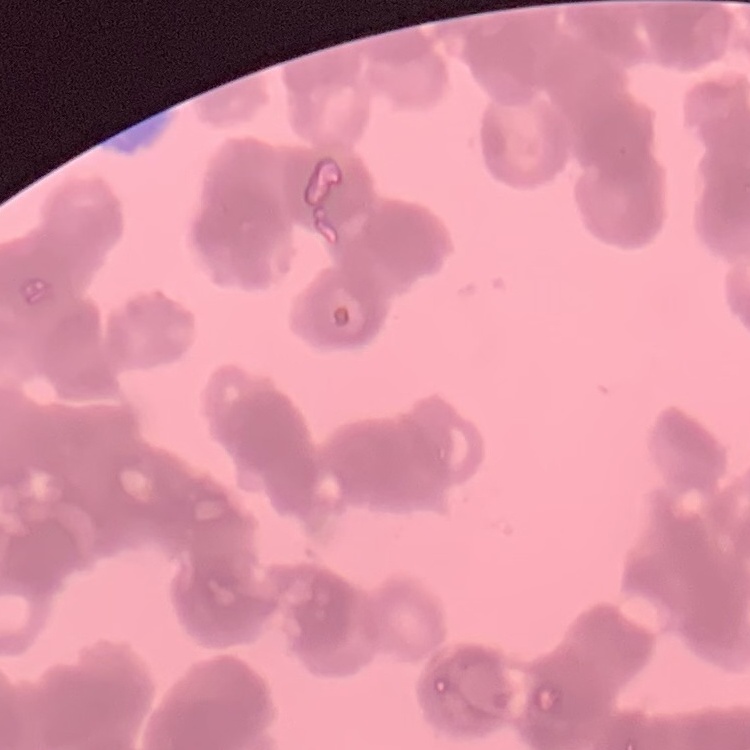

The red blood cells show rouleaux formation. One tile cut from a larger photomicrograph. Field's or Giemsa stain. Thin blood film.